Classify this cell by malaria status.
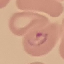

Parasitized.

capture = smartphone through the microscope eyepiece
image type = automatically extracted cell patch, resized to 64 × 64 pixels
stain = Giemsa
preparation = thin blood smear